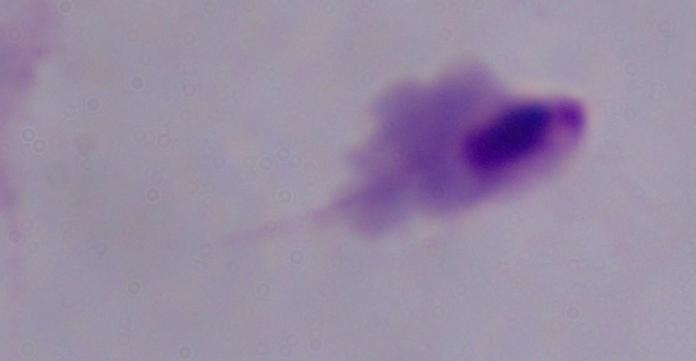
modality = micrograph
magnification = 1000x
identification = trichomonad